Report the malaria status of this cell.
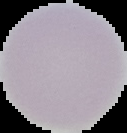

Uninfected.

From a thin blood smear. Image is 127×133 pixels. The area outside the segmented cell region is set to black.